State which parasite is depicted.
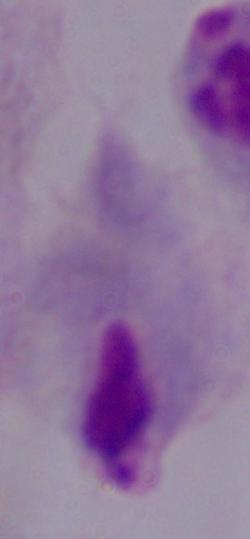
A trichomonad.

Summary:
  - Magnification: 1000x
  - Modality: photomicrograph